Locate every blood parasite and identify its species.
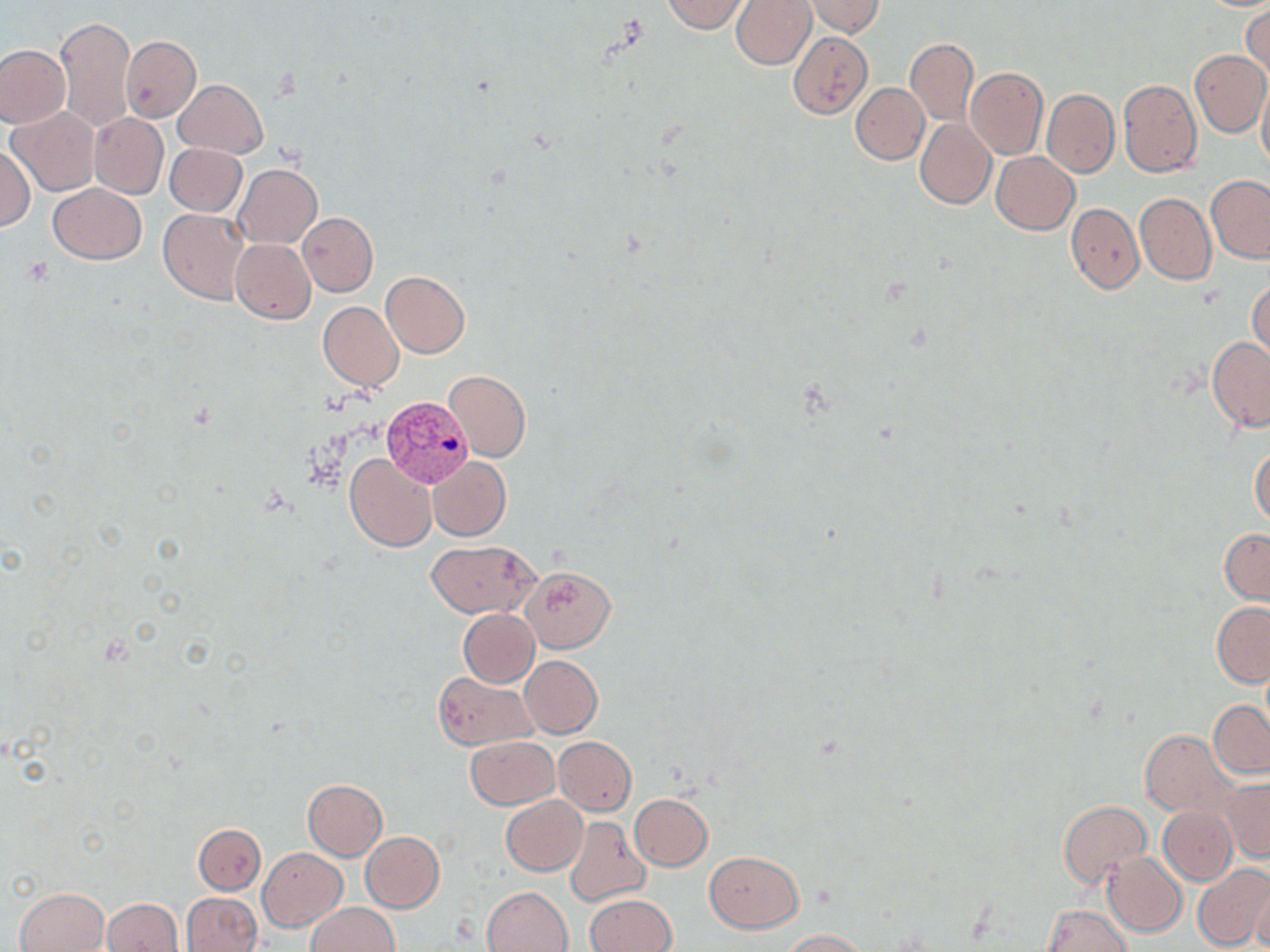

Approximate bounding boxes as (x1, y1, x2, y2) in pixels.
Plasmodium vivax-infected red blood cells: (381, 395, 473, 488).
No Plasmodium falciparum, Plasmodium ovale, Plasmodium malariae, Babesia divergens, or Trypanosoma brucei observed.

Summary:
  - Uninfected red blood cell locations: (661, 0, 751, 33), (731, 0, 816, 69), (805, 0, 883, 37), (1201, 1, 1270, 11), (1242, 5, 1269, 80), (56, 15, 136, 131), (787, 30, 872, 119), (121, 36, 201, 122), (904, 39, 979, 125), (0, 44, 69, 127), (1189, 50, 1270, 137), (964, 68, 1048, 161), (172, 78, 267, 158), (1258, 78, 1270, 175), (1118, 80, 1202, 177), (851, 83, 930, 165), (1042, 88, 1119, 178), (7, 106, 101, 196), (89, 113, 168, 199), (915, 119, 996, 209), (164, 143, 247, 216), (0, 146, 34, 232), (992, 152, 1080, 234), (234, 164, 322, 248), (1206, 174, 1270, 263), (48, 183, 145, 265), (1135, 193, 1215, 285), (1066, 203, 1144, 294), (159, 209, 250, 304), (297, 212, 378, 296), (231, 239, 316, 324), (380, 272, 469, 357), (1249, 280, 1270, 361), (317, 302, 404, 390), (1206, 336, 1270, 432), (443, 370, 531, 462), (1250, 444, 1270, 529), (345, 453, 436, 552), (428, 456, 510, 540), (1220, 528, 1270, 605), (425, 539, 538, 618), (519, 565, 614, 651), (1212, 601, 1270, 686), (457, 608, 539, 687), (519, 655, 602, 737), (433, 672, 537, 751), (1208, 701, 1269, 778), (1140, 729, 1236, 818), (466, 736, 558, 809), (553, 736, 635, 815), (1223, 779, 1270, 861), (302, 780, 387, 861), (629, 793, 713, 871), (501, 796, 587, 875), (1058, 800, 1151, 886), (1158, 805, 1237, 885), (565, 816, 651, 907), (193, 823, 265, 893), (360, 831, 444, 912), (258, 847, 347, 930), (705, 851, 804, 932), (1103, 851, 1187, 937), (1192, 864, 1270, 952), (1251, 877, 1270, 952), (483, 886, 572, 952), (14, 887, 109, 952), (181, 892, 262, 952), (585, 894, 676, 952), (101, 898, 184, 951), (306, 902, 400, 952), (1042, 905, 1130, 952), (779, 929, 869, 951)
  - Slide-level diagnosis: Plasmodium vivax
  - Field of view: single
  - Magnification: 1000x
  - Stain: May-Grünwald-Giemsa
  - Image size: 1270×952 pixels
  - Preparation: thin blood smear
  - Modality: optical microscopy